Assess the morphology of the red blood cells.
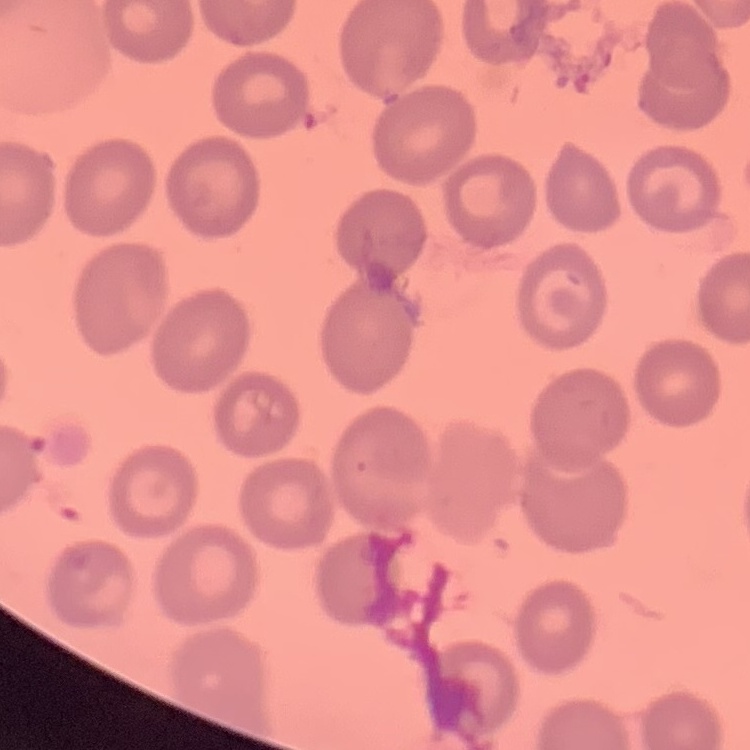

They show no rouleaux formation.

Field's or Giemsa stain. One tile cut from a larger photomicrograph. Thin peripheral smear.